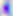

magnification = 400x
modality = micrograph
identification = Toxoplasma gondii